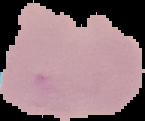

Summary:
  - Image type: cell region segmented out of the field of view; surrounding area masked to black
  - Preparation: thin blood film
  - Image size: 145×121 pixels
  - Malaria status: uninfected